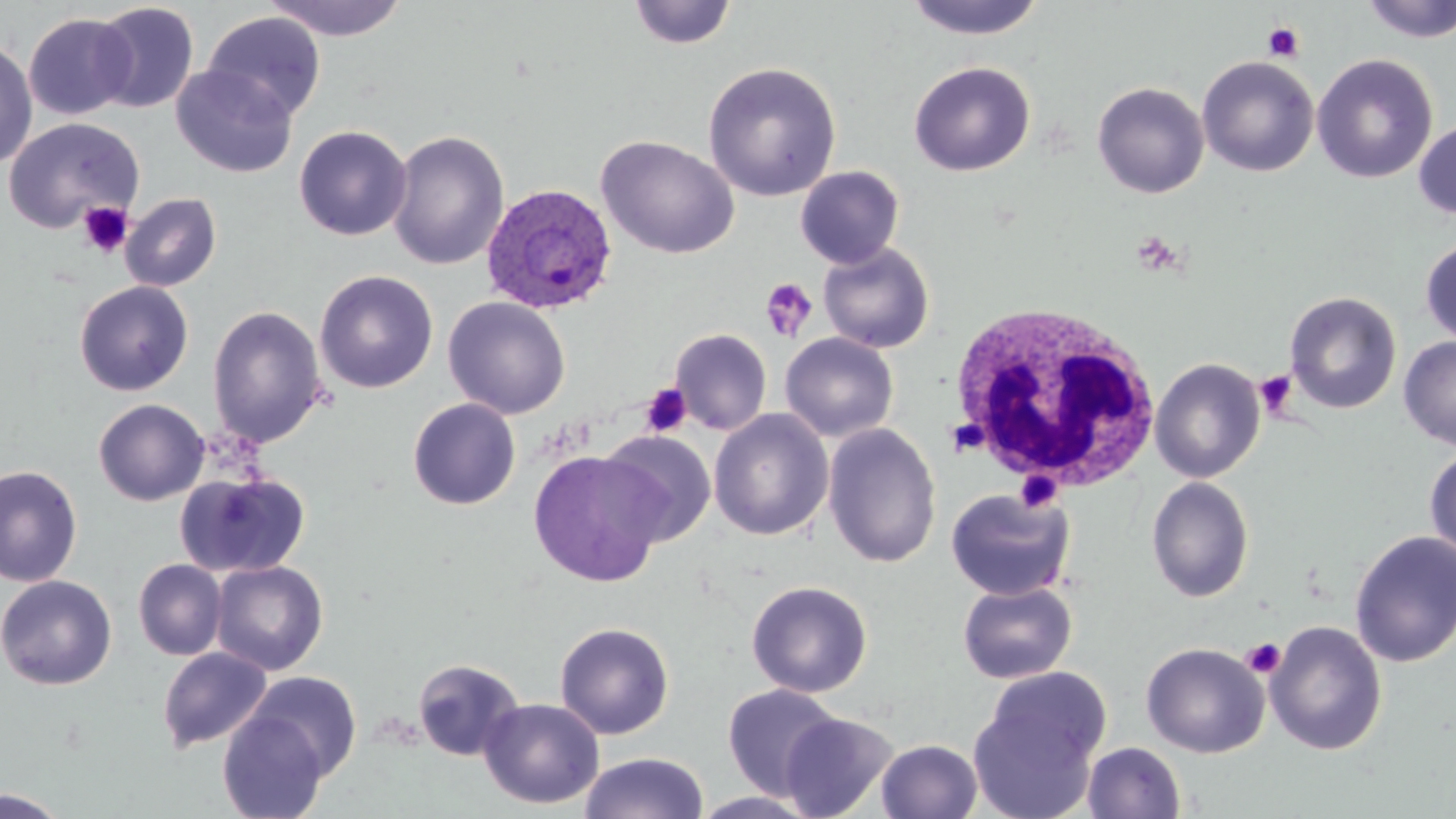
slide-level diagnosis = Plasmodium ovale
preparation = thin blood smear
white blood cell locations = approximate bounding boxes as named x1/y1/x2/y2 corners in pixels: (x1=944, y1=306, x2=1167, y2=494)
modality = optical microscopy
uninfected red blood cell locations = approximate bounding boxes as named x1/y1/x2/y2 corners in pixels: (x1=262, y1=0, x2=410, y2=41), (x1=1360, y1=0, x2=1456, y2=43), (x1=91, y1=1, x2=199, y2=114), (x1=627, y1=1, x2=737, y2=49), (x1=902, y1=1, x2=1048, y2=40), (x1=201, y1=11, x2=327, y2=124), (x1=23, y1=13, x2=137, y2=121), (x1=0, y1=37, x2=38, y2=170), (x1=1312, y1=53, x2=1438, y2=184), (x1=1197, y1=56, x2=1320, y2=177), (x1=702, y1=61, x2=841, y2=201), (x1=909, y1=61, x2=1036, y2=177), (x1=172, y1=65, x2=298, y2=178), (x1=1092, y1=81, x2=1210, y2=199), (x1=2, y1=117, x2=143, y2=234), (x1=1414, y1=119, x2=1456, y2=219), (x1=294, y1=125, x2=412, y2=241), (x1=387, y1=130, x2=509, y2=271), (x1=596, y1=134, x2=739, y2=260), (x1=795, y1=166, x2=905, y2=268), (x1=120, y1=193, x2=222, y2=292), (x1=1420, y1=236, x2=1456, y2=348), (x1=818, y1=242, x2=935, y2=353), (x1=314, y1=270, x2=438, y2=393), (x1=74, y1=280, x2=193, y2=396), (x1=1283, y1=291, x2=1402, y2=414), (x1=443, y1=296, x2=571, y2=419), (x1=207, y1=305, x2=328, y2=448), (x1=670, y1=329, x2=771, y2=435), (x1=779, y1=332, x2=899, y2=442), (x1=1398, y1=336, x2=1456, y2=450), (x1=1149, y1=358, x2=1266, y2=482), (x1=93, y1=398, x2=210, y2=506), (x1=407, y1=398, x2=521, y2=510), (x1=709, y1=409, x2=834, y2=540), (x1=822, y1=423, x2=941, y2=568), (x1=599, y1=429, x2=716, y2=546), (x1=1424, y1=446, x2=1456, y2=563), (x1=528, y1=450, x2=667, y2=586), (x1=0, y1=464, x2=83, y2=586), (x1=175, y1=470, x2=310, y2=578), (x1=1145, y1=476, x2=1255, y2=602), (x1=945, y1=488, x2=1075, y2=600), (x1=1349, y1=530, x2=1456, y2=668), (x1=134, y1=559, x2=227, y2=660), (x1=210, y1=560, x2=328, y2=675), (x1=0, y1=574, x2=117, y2=691), (x1=957, y1=579, x2=1077, y2=684), (x1=746, y1=580, x2=873, y2=698), (x1=1265, y1=621, x2=1387, y2=756), (x1=554, y1=622, x2=675, y2=740), (x1=1141, y1=642, x2=1269, y2=758), (x1=157, y1=646, x2=272, y2=752), (x1=412, y1=658, x2=524, y2=762), (x1=245, y1=671, x2=363, y2=781), (x1=969, y1=672, x2=1108, y2=817), (x1=722, y1=683, x2=844, y2=800), (x1=478, y1=697, x2=604, y2=809), (x1=218, y1=709, x2=330, y2=819), (x1=779, y1=711, x2=898, y2=819), (x1=876, y1=739, x2=982, y2=819), (x1=1082, y1=741, x2=1186, y2=819), (x1=580, y1=751, x2=709, y2=819), (x1=1, y1=788, x2=70, y2=818), (x1=690, y1=791, x2=820, y2=818)
stain = May-Grünwald-Giemsa
magnification = 1000x
Plasmodium ovale-infected red blood cell locations = approximate bounding boxes as named x1/y1/x2/y2 corners in pixels: (x1=481, y1=182, x2=618, y2=315)
field of view = single
platelet locations = approximate bounding boxes as named x1/y1/x2/y2 corners in pixels: (x1=1262, y1=21, x2=1305, y2=62), (x1=77, y1=200, x2=133, y2=259), (x1=1131, y1=230, x2=1184, y2=277), (x1=759, y1=276, x2=819, y2=342), (x1=1255, y1=370, x2=1297, y2=417), (x1=640, y1=383, x2=692, y2=437), (x1=1014, y1=470, x2=1063, y2=513), (x1=1241, y1=638, x2=1286, y2=679)
image size = 1456×819 pixels